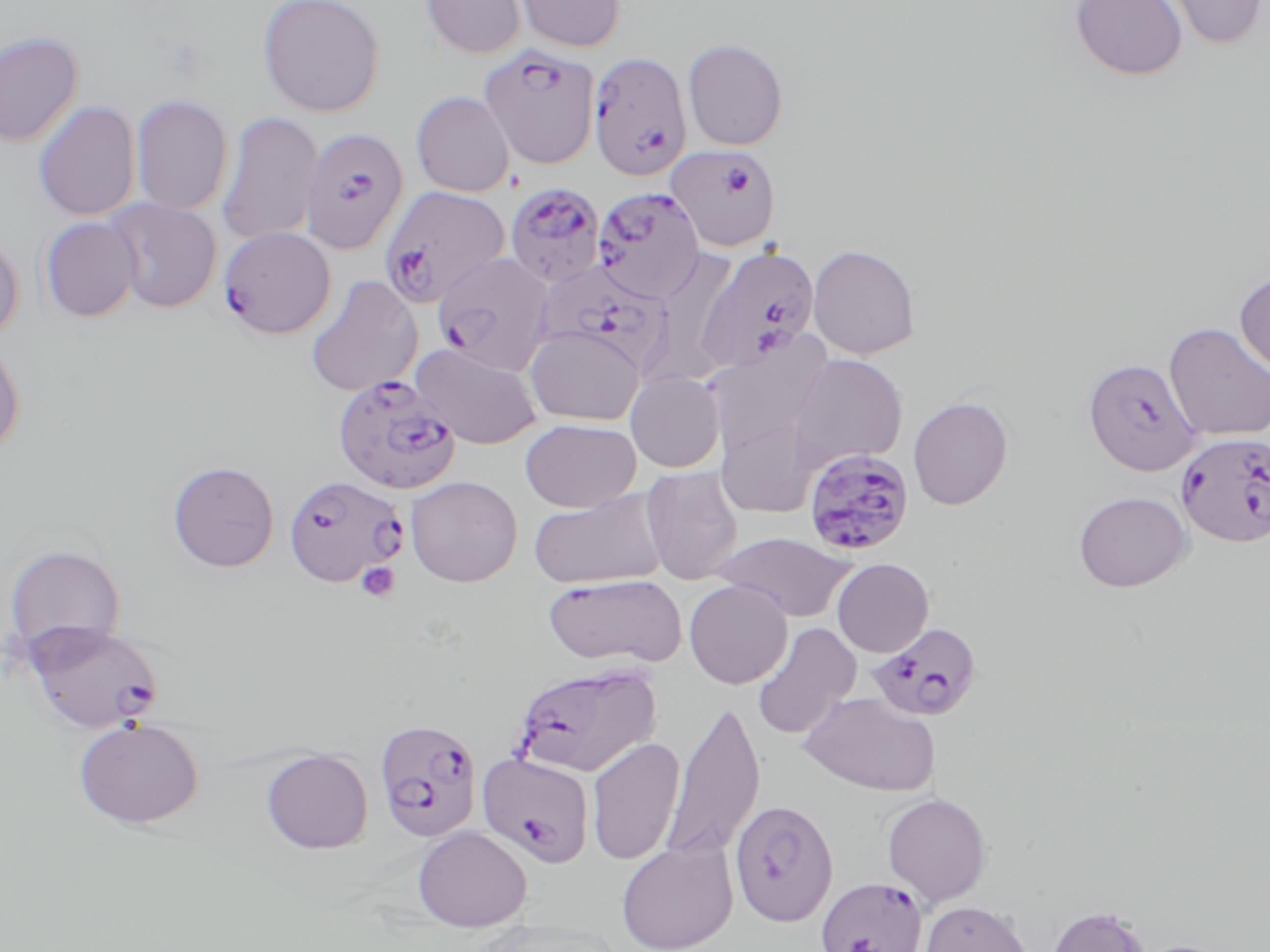
Approximate bounding boxes as (x1,y1)-(x2,y2) corner pairs in pixels. Platelet locations: (357,562)-(401,602). Uninfected red blood cell locations: (256,0)-(386,117), (420,0)-(527,60), (514,0)-(626,53), (1070,0)-(1189,81), (1156,0)-(1268,50), (0,30)-(85,146), (682,38)-(789,151), (410,91)-(515,197), (130,94)-(233,215), (33,100)-(141,221), (216,111)-(324,245), (105,197)-(223,313), (39,216)-(142,322), (0,229)-(24,343), (807,243)-(921,360), (657,249)-(742,373), (1234,271)-(1270,377), (305,274)-(423,397), (1164,322)-(1270,440), (525,325)-(645,426), (705,333)-(836,458), (0,335)-(26,459), (410,342)-(542,449), (788,353)-(908,471), (625,370)-(725,473), (907,395)-(1014,510), (715,416)-(818,518), (520,418)-(641,512), (167,460)-(280,573), (639,465)-(744,584), (405,475)-(523,587), (528,487)-(669,589), (1073,490)-(1192,592), (713,533)-(858,622), (4,544)-(126,655), (831,558)-(934,657), (684,579)-(792,690), (752,623)-(861,739), (800,691)-(941,796), (664,700)-(765,863), (72,717)-(205,831), (586,736)-(685,865), (261,748)-(373,854), (881,792)-(993,908), (413,825)-(532,932), (616,840)-(737,952), (918,900)-(1032,952), (1046,905)-(1153,952), (1130,939)-(1241,952). Plasmodium falciparum-infected red blood cell locations: (478,45)-(600,170), (588,51)-(692,181), (300,128)-(409,254), (665,144)-(782,253), (503,183)-(606,289), (378,185)-(510,308), (591,186)-(706,303), (218,226)-(337,339), (693,245)-(821,375), (433,252)-(555,373), (533,260)-(670,370), (1082,357)-(1203,476), (333,373)-(462,495), (1175,431)-(1270,548), (803,447)-(915,556), (284,474)-(408,587), (543,573)-(686,668), (19,620)-(166,736), (866,621)-(984,723), (512,662)-(661,777), (373,717)-(481,843), (477,752)-(595,867), (729,799)-(839,927), (815,875)-(927,952). Slide-level diagnosis: Plasmodium falciparum. May-Grünwald-Giemsa-stained preparation. Optical microscopy. Thin blood film. One field of a larger specimen. 1000x magnification. Image is 1270×952 pixels.